Outline each Plasmodium falciparum-infected red blood cell.
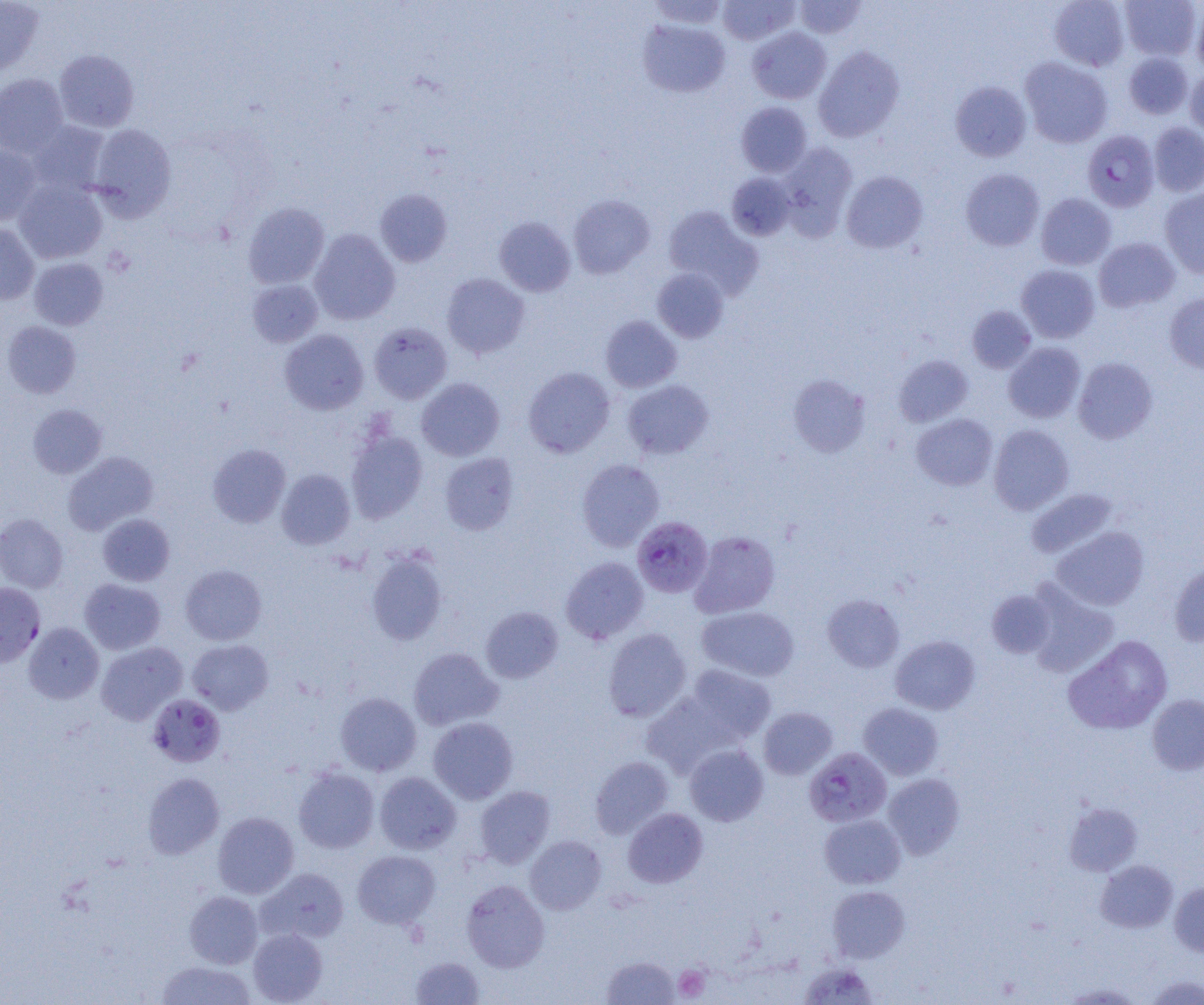

Approximate bounding boxes as named x1/y1/x2/y2 corners in pixels.
Plasmodium falciparum-infected red blood cells: (x1=1082, y1=130, x2=1159, y2=212), (x1=631, y1=516, x2=713, y2=597), (x1=0, y1=583, x2=45, y2=667), (x1=148, y1=694, x2=225, y2=767), (x1=804, y1=747, x2=892, y2=827).

slide-level diagnosis = Plasmodium falciparum
platelet locations = approximate bounding boxes as named x1/y1/x2/y2 corners in pixels: (x1=673, y1=965, x2=710, y2=1001)
preparation = thin blood smear
modality = light microscopy
uninfected red blood cell locations = approximate bounding boxes as named x1/y1/x2/y2 corners in pixels: (x1=0, y1=0, x2=43, y2=77), (x1=647, y1=0, x2=728, y2=30), (x1=717, y1=0, x2=799, y2=45), (x1=1049, y1=0, x2=1130, y2=70), (x1=1120, y1=0, x2=1201, y2=61), (x1=794, y1=1, x2=866, y2=39), (x1=1192, y1=6, x2=1204, y2=74), (x1=637, y1=19, x2=730, y2=97), (x1=747, y1=27, x2=831, y2=104), (x1=814, y1=46, x2=905, y2=142), (x1=54, y1=49, x2=139, y2=132), (x1=1123, y1=52, x2=1193, y2=119), (x1=1020, y1=57, x2=1113, y2=148), (x1=1185, y1=68, x2=1204, y2=140), (x1=0, y1=73, x2=69, y2=157), (x1=950, y1=81, x2=1031, y2=161), (x1=736, y1=102, x2=812, y2=177), (x1=27, y1=121, x2=110, y2=197), (x1=1148, y1=122, x2=1204, y2=197), (x1=88, y1=124, x2=177, y2=221), (x1=778, y1=142, x2=857, y2=236), (x1=0, y1=144, x2=42, y2=225), (x1=960, y1=168, x2=1044, y2=250), (x1=841, y1=170, x2=928, y2=253), (x1=726, y1=172, x2=795, y2=240), (x1=14, y1=179, x2=108, y2=264), (x1=375, y1=188, x2=452, y2=267), (x1=1160, y1=188, x2=1204, y2=277), (x1=1036, y1=193, x2=1116, y2=270), (x1=568, y1=194, x2=655, y2=279), (x1=243, y1=202, x2=330, y2=289), (x1=662, y1=206, x2=762, y2=297), (x1=494, y1=216, x2=575, y2=296), (x1=0, y1=223, x2=39, y2=304), (x1=309, y1=228, x2=400, y2=325), (x1=1094, y1=238, x2=1180, y2=312), (x1=29, y1=257, x2=108, y2=330), (x1=1016, y1=264, x2=1099, y2=343), (x1=651, y1=268, x2=729, y2=343), (x1=441, y1=273, x2=530, y2=358), (x1=247, y1=279, x2=323, y2=348), (x1=1164, y1=293, x2=1204, y2=374), (x1=967, y1=306, x2=1036, y2=373), (x1=600, y1=315, x2=682, y2=392), (x1=2, y1=320, x2=81, y2=398), (x1=369, y1=321, x2=453, y2=403), (x1=279, y1=329, x2=368, y2=414), (x1=1003, y1=342, x2=1086, y2=423), (x1=894, y1=355, x2=973, y2=427), (x1=1073, y1=357, x2=1158, y2=443), (x1=523, y1=366, x2=615, y2=458), (x1=787, y1=374, x2=870, y2=457), (x1=416, y1=378, x2=505, y2=461), (x1=622, y1=379, x2=714, y2=459), (x1=28, y1=404, x2=107, y2=478), (x1=912, y1=414, x2=997, y2=490), (x1=989, y1=424, x2=1074, y2=515), (x1=345, y1=428, x2=427, y2=523), (x1=207, y1=443, x2=290, y2=527), (x1=62, y1=451, x2=159, y2=535), (x1=440, y1=453, x2=519, y2=535), (x1=577, y1=459, x2=664, y2=551), (x1=277, y1=469, x2=355, y2=549), (x1=1026, y1=488, x2=1120, y2=560), (x1=0, y1=513, x2=68, y2=593), (x1=97, y1=513, x2=175, y2=586), (x1=1050, y1=526, x2=1149, y2=611), (x1=690, y1=530, x2=780, y2=618), (x1=366, y1=549, x2=448, y2=646), (x1=561, y1=557, x2=649, y2=644), (x1=1169, y1=562, x2=1204, y2=647), (x1=180, y1=564, x2=267, y2=645), (x1=79, y1=579, x2=165, y2=654), (x1=1025, y1=583, x2=1119, y2=677), (x1=986, y1=590, x2=1056, y2=657), (x1=822, y1=594, x2=905, y2=672), (x1=481, y1=606, x2=563, y2=683), (x1=696, y1=606, x2=799, y2=681), (x1=23, y1=622, x2=103, y2=704), (x1=603, y1=628, x2=691, y2=721), (x1=890, y1=635, x2=980, y2=715), (x1=1063, y1=635, x2=1172, y2=735), (x1=187, y1=639, x2=274, y2=715), (x1=96, y1=642, x2=187, y2=725), (x1=408, y1=647, x2=503, y2=730), (x1=684, y1=665, x2=776, y2=744), (x1=335, y1=692, x2=421, y2=776), (x1=641, y1=692, x2=735, y2=776), (x1=1147, y1=694, x2=1204, y2=775), (x1=858, y1=703, x2=943, y2=780), (x1=759, y1=707, x2=837, y2=779), (x1=428, y1=717, x2=518, y2=803), (x1=684, y1=744, x2=768, y2=826), (x1=590, y1=756, x2=674, y2=839), (x1=293, y1=766, x2=380, y2=853), (x1=142, y1=772, x2=224, y2=859), (x1=375, y1=772, x2=461, y2=854), (x1=883, y1=773, x2=965, y2=859), (x1=475, y1=786, x2=555, y2=868), (x1=1063, y1=802, x2=1143, y2=876), (x1=623, y1=808, x2=708, y2=888), (x1=213, y1=812, x2=299, y2=899), (x1=820, y1=814, x2=906, y2=889), (x1=525, y1=835, x2=606, y2=914), (x1=352, y1=850, x2=440, y2=929), (x1=1095, y1=860, x2=1178, y2=933), (x1=256, y1=868, x2=349, y2=945), (x1=462, y1=880, x2=549, y2=972), (x1=1169, y1=881, x2=1204, y2=957), (x1=828, y1=886, x2=910, y2=963), (x1=184, y1=891, x2=263, y2=968), (x1=248, y1=928, x2=327, y2=1004), (x1=411, y1=956, x2=485, y2=1004), (x1=601, y1=956, x2=681, y2=1004), (x1=155, y1=959, x2=256, y2=1004), (x1=799, y1=961, x2=880, y2=1004), (x1=1144, y1=975, x2=1204, y2=1004), (x1=1061, y1=983, x2=1143, y2=1004)
image size = 1204×1005 pixels
field of view = one of a larger specimen
magnification = 1000x